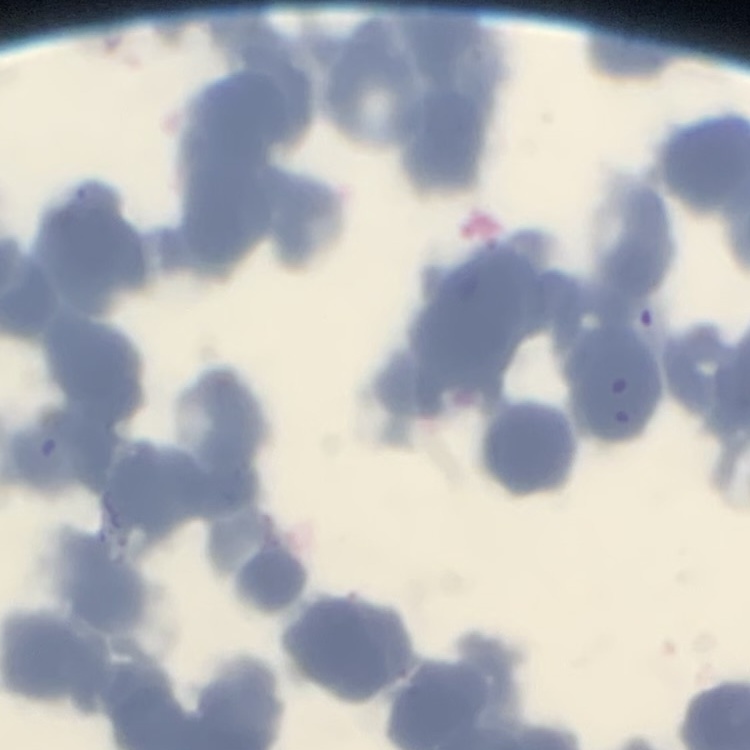

red blood cell morphology = rouleaux formation
stain = Field's or Giemsa
image type = square crop of a larger photomicrograph
preparation = thin peripheral smear